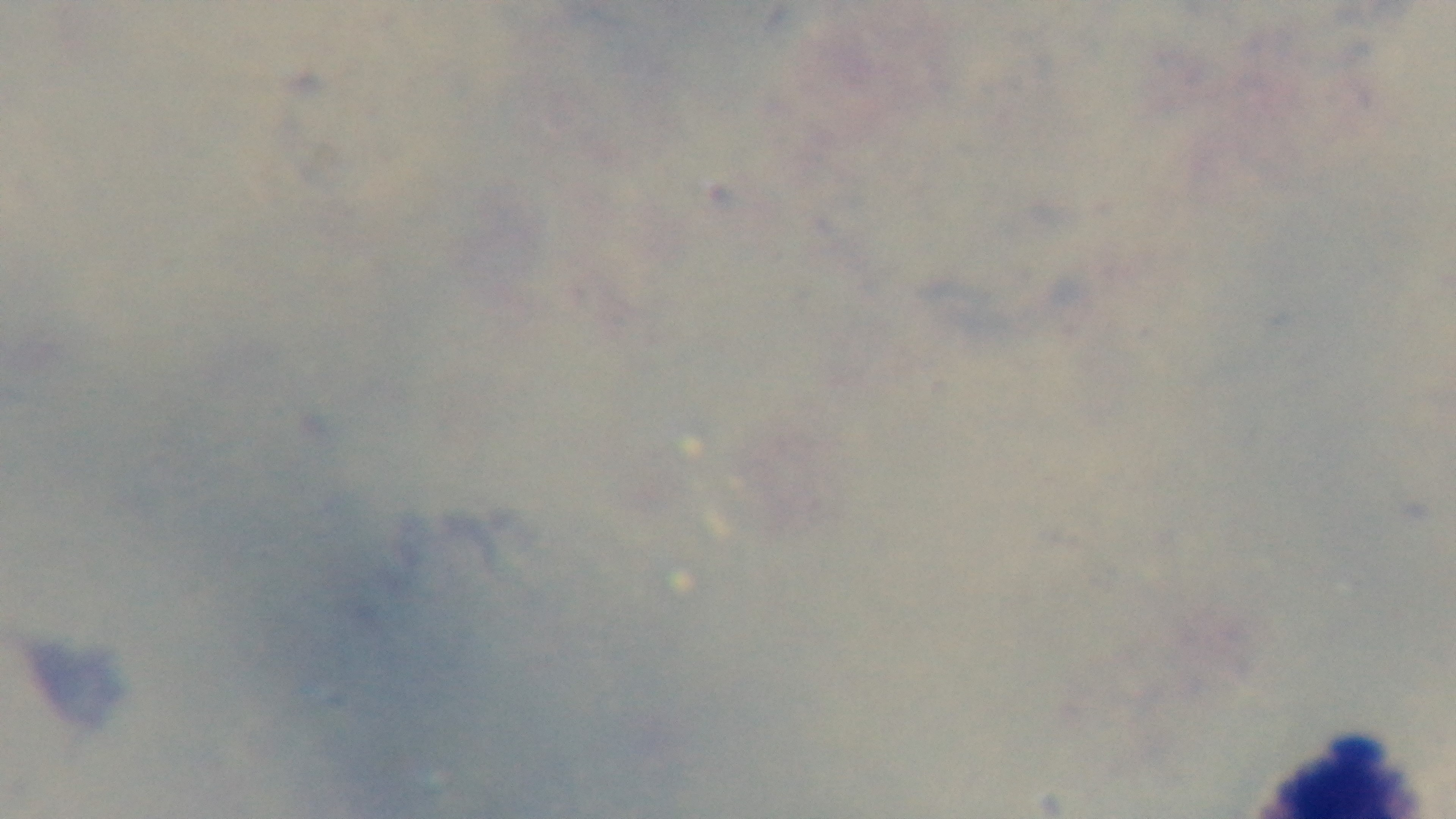
Summary:
  - Preparation: thick
  - Modality: light microscopy
  - Malaria status: uninfected
  - Capture: mounted 4K digital camera
  - Field of view: one from the slide
  - Objective: 100x oil immersion
  - Stain: Giemsa